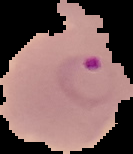
Malaria status: parasitized. From a thin blood smear. The area outside the segmented cell region is set to black. Image is 133×154 pixels.